Comment on the morphology of the red blood cells.
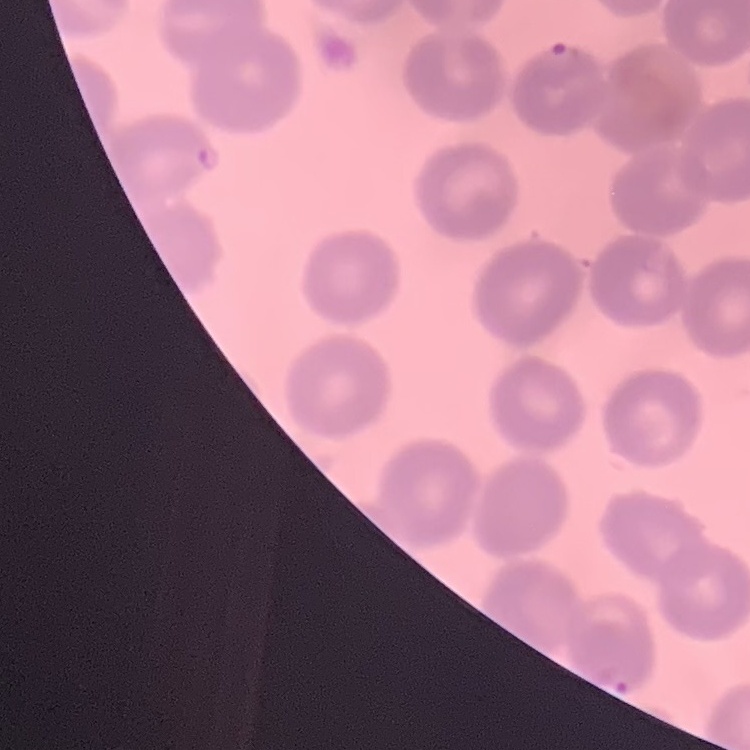
They show no rouleaux formation.

Thin blood smear. One tile cut from a larger photomicrograph. Field's or Giemsa stain.